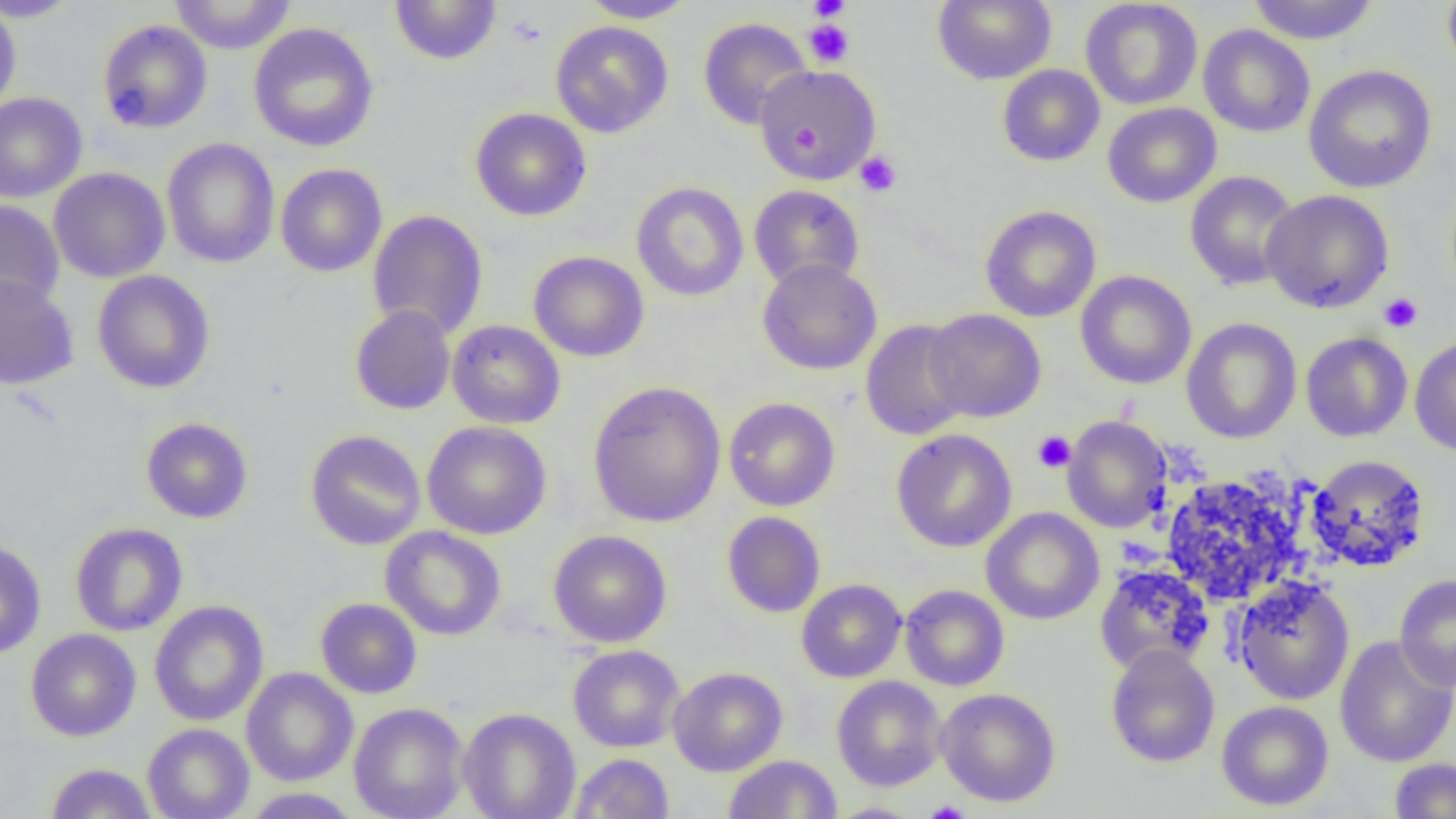
Summary:
  - Coordinate format: approximate bounding boxes as named x1/y1/x2/y2 corners in pixels
  - Platelet locations: (x1=807, y1=0, x2=851, y2=21), (x1=803, y1=19, x2=855, y2=68), (x1=855, y1=151, x2=902, y2=196), (x1=1379, y1=293, x2=1423, y2=333), (x1=1033, y1=430, x2=1076, y2=473), (x1=924, y1=802, x2=970, y2=819)
  - Uninfected red blood cell locations: (x1=0, y1=0, x2=82, y2=22), (x1=168, y1=0, x2=297, y2=54), (x1=579, y1=0, x2=697, y2=23), (x1=932, y1=0, x2=1056, y2=85), (x1=1080, y1=0, x2=1203, y2=110), (x1=1246, y1=0, x2=1380, y2=45), (x1=1442, y1=0, x2=1456, y2=82), (x1=389, y1=1, x2=502, y2=66), (x1=0, y1=2, x2=22, y2=117), (x1=698, y1=18, x2=812, y2=130), (x1=97, y1=19, x2=213, y2=134), (x1=550, y1=21, x2=673, y2=138), (x1=248, y1=22, x2=379, y2=152), (x1=1198, y1=24, x2=1315, y2=138), (x1=1303, y1=64, x2=1437, y2=193), (x1=754, y1=65, x2=882, y2=184), (x1=997, y1=65, x2=1105, y2=166), (x1=0, y1=92, x2=88, y2=203), (x1=1103, y1=102, x2=1221, y2=208), (x1=470, y1=107, x2=592, y2=222), (x1=161, y1=138, x2=280, y2=268), (x1=275, y1=163, x2=387, y2=277), (x1=48, y1=167, x2=170, y2=283), (x1=1185, y1=171, x2=1300, y2=292), (x1=631, y1=182, x2=749, y2=302), (x1=748, y1=184, x2=865, y2=290), (x1=1260, y1=189, x2=1394, y2=314), (x1=0, y1=200, x2=65, y2=310), (x1=980, y1=205, x2=1101, y2=322), (x1=367, y1=210, x2=488, y2=340), (x1=528, y1=251, x2=649, y2=362), (x1=757, y1=258, x2=882, y2=376), (x1=92, y1=270, x2=215, y2=394), (x1=1075, y1=270, x2=1197, y2=389), (x1=0, y1=274, x2=79, y2=390), (x1=350, y1=304, x2=456, y2=415), (x1=923, y1=309, x2=1047, y2=422), (x1=1181, y1=318, x2=1302, y2=444), (x1=447, y1=320, x2=565, y2=429), (x1=860, y1=320, x2=973, y2=441), (x1=1300, y1=332, x2=1413, y2=442), (x1=1409, y1=335, x2=1456, y2=457), (x1=588, y1=381, x2=726, y2=527), (x1=724, y1=397, x2=840, y2=512), (x1=1062, y1=416, x2=1172, y2=533), (x1=140, y1=417, x2=253, y2=523), (x1=422, y1=421, x2=551, y2=540), (x1=891, y1=429, x2=1017, y2=552), (x1=305, y1=430, x2=426, y2=550), (x1=1306, y1=454, x2=1431, y2=572), (x1=1162, y1=474, x2=1303, y2=605), (x1=981, y1=507, x2=1105, y2=625), (x1=721, y1=511, x2=826, y2=617), (x1=69, y1=522, x2=188, y2=636), (x1=380, y1=525, x2=506, y2=641), (x1=548, y1=530, x2=672, y2=648), (x1=0, y1=540, x2=46, y2=658), (x1=1094, y1=563, x2=1215, y2=676), (x1=1394, y1=573, x2=1456, y2=691), (x1=1232, y1=576, x2=1355, y2=706), (x1=796, y1=579, x2=907, y2=683), (x1=900, y1=584, x2=1010, y2=691), (x1=315, y1=598, x2=422, y2=699), (x1=149, y1=600, x2=268, y2=726), (x1=25, y1=628, x2=141, y2=742), (x1=1334, y1=635, x2=1456, y2=768), (x1=568, y1=644, x2=685, y2=752), (x1=1105, y1=644, x2=1220, y2=768), (x1=241, y1=667, x2=358, y2=786), (x1=668, y1=667, x2=788, y2=776), (x1=831, y1=675, x2=947, y2=792), (x1=935, y1=688, x2=1061, y2=807), (x1=1216, y1=700, x2=1334, y2=811), (x1=348, y1=702, x2=469, y2=819), (x1=457, y1=708, x2=580, y2=819), (x1=142, y1=723, x2=254, y2=819), (x1=569, y1=752, x2=674, y2=818), (x1=723, y1=754, x2=842, y2=818), (x1=1388, y1=758, x2=1456, y2=818), (x1=44, y1=762, x2=158, y2=818), (x1=240, y1=787, x2=363, y2=818), (x1=824, y1=803, x2=926, y2=819)
  - Slide-level diagnosis: negative for blood parasites
  - Field of view: single
  - Image size: 1456×819 pixels
  - Modality: optical microscopy
  - Preparation: thin blood film
  - Magnification: 1000x